Locate every leukocyte (white blood cell).
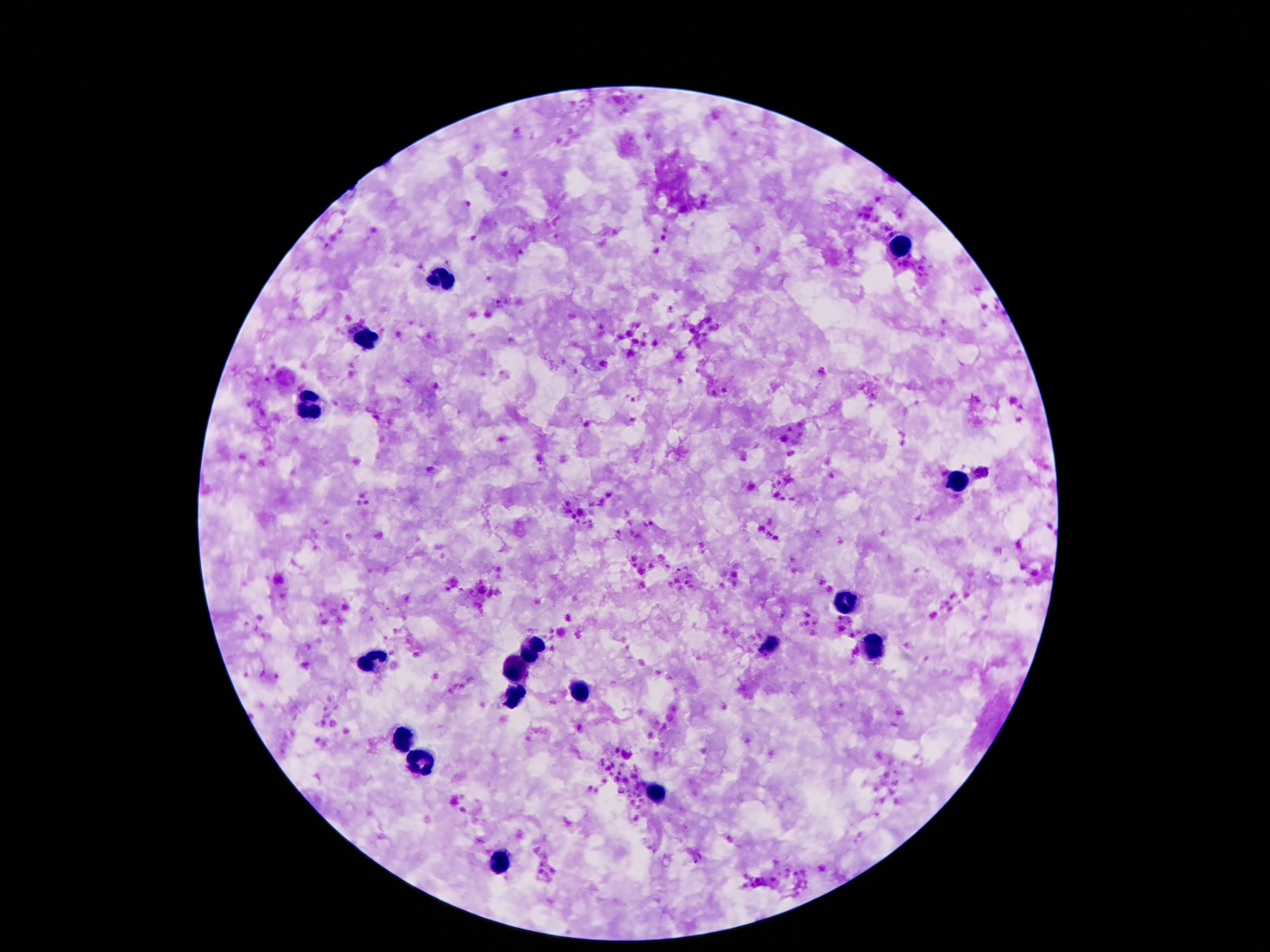

Approximate centers as (x, y) in pixels.
Leukocytes: (901, 242), (439, 278), (366, 337), (309, 409), (954, 482), (846, 601), (534, 646), (765, 648), (877, 648), (371, 666), (517, 670), (581, 690), (514, 697), (402, 737), (422, 762), (655, 794), (506, 861).

Smartphone photograph taken through the microscope eyepiece. Image is 1270×952 pixels. Giemsa-stained preparation. Patient malaria status: not infected. One field from this slide. Thick peripheral-blood smear. 100x magnification.